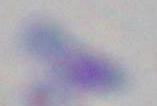

Summary:
  - Magnification: 1000x
  - Identification: Toxoplasma gondii
  - Modality: photomicrograph